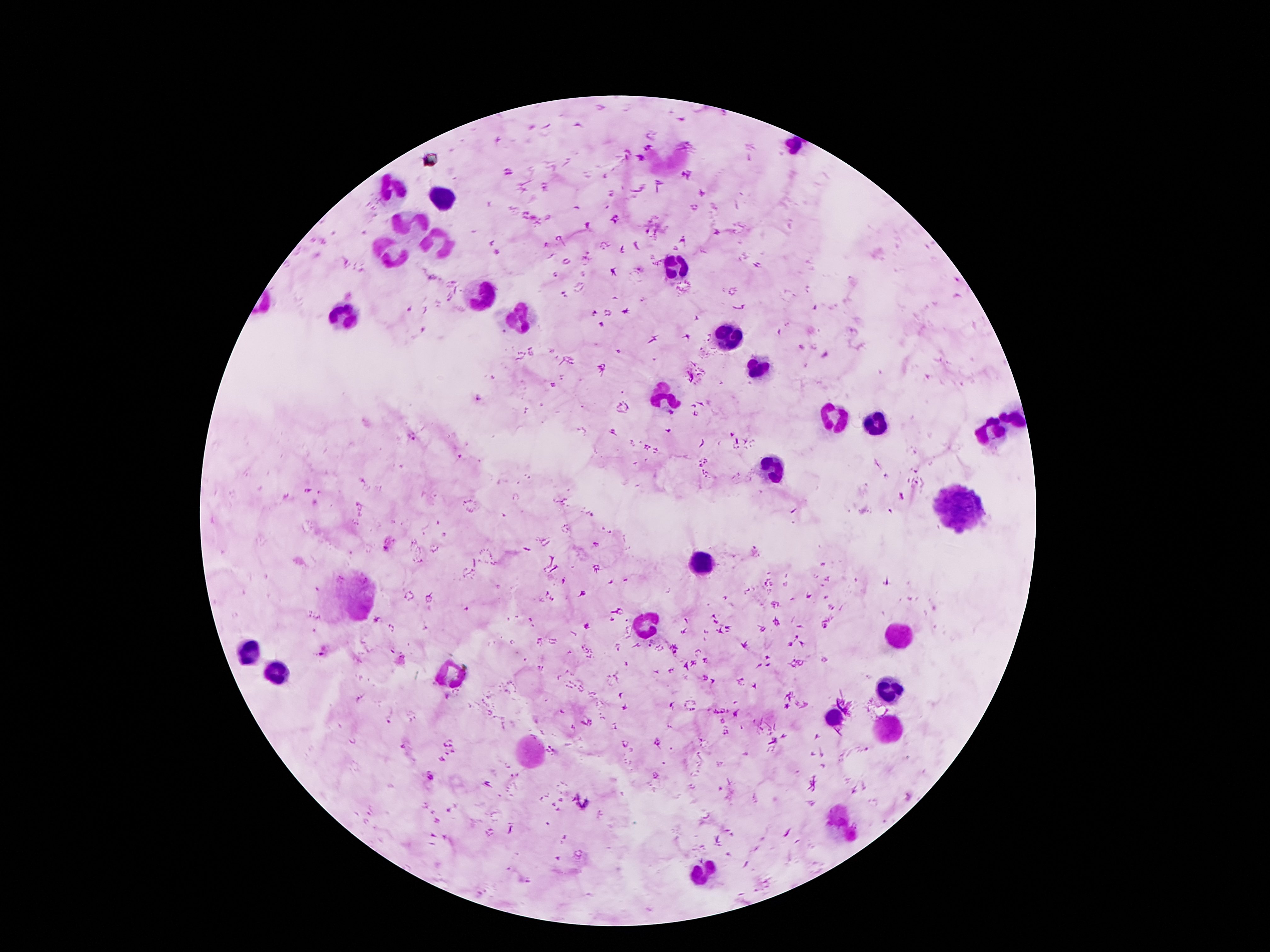
coordinate format = approximate centers as [x, y] in pixels
malaria parasite locations = [479, 398], [411, 436], [900, 497], [384, 549], [327, 651], [447, 697], [428, 777]
leukocyte locations = [390, 191], [437, 200], [413, 220], [443, 243], [392, 255], [677, 269], [488, 294], [345, 318], [511, 320], [726, 337], [763, 368], [665, 398], [837, 419], [1015, 419], [876, 425], [992, 439], [775, 468], [958, 507], [703, 564], [353, 601], [646, 624], [892, 634], [247, 653], [277, 673], [451, 673], [886, 692], [833, 716], [886, 728], [529, 751], [839, 821], [705, 874]
field of view = one from this slide
preparation = thick peripheral-blood smear
capture = smartphone camera through the microscope eyepiece
magnification = 100x
image size = 1270×952 pixels
stain = Giemsa
patient malaria status = infected with Plasmodium falciparum